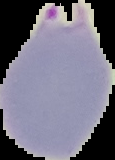

Summary:
  - Preparation: thin blood film
  - Image size: 115×160 pixels
  - Malaria status: parasitized
  - Image type: segmented cell region on a black background